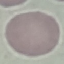

result: negative for malaria parasites
capture: smartphone through the microscope eyepiece
stain: Giemsa
image_type: cell patch, automatically extracted from a larger field of view and resized to 64 × 64 pixels
preparation: thin blood film